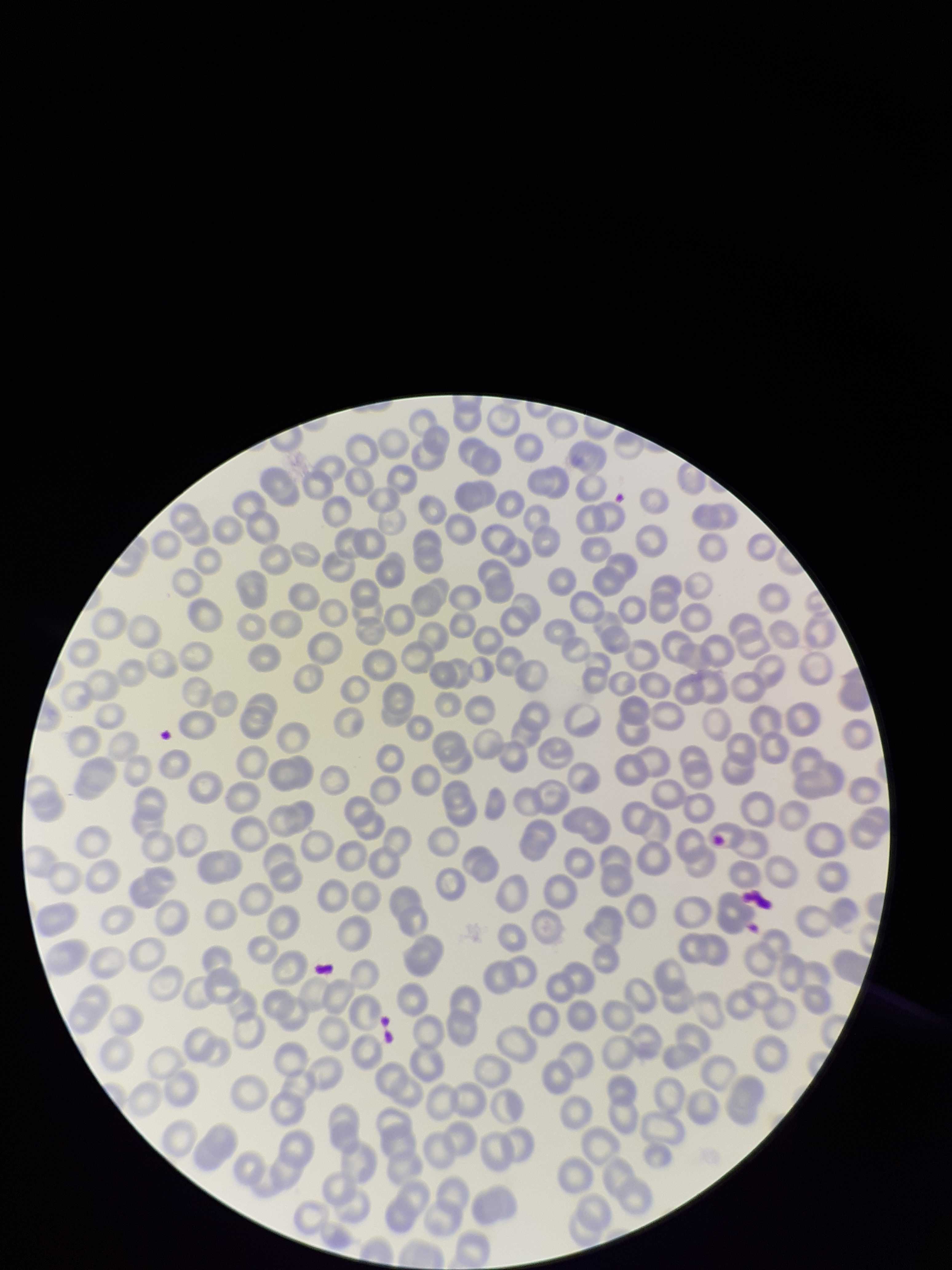 Parasitized red blood cell count: 0. Preparation: thin blood smear. Image is 952×1270 pixels. Giemsa stain. Parasitized red blood cells: none detected. Patient malaria status: negative. Red blood cell count: 242. Photographed through the microscope eyepiece with a smartphone camera. One field from this slide.